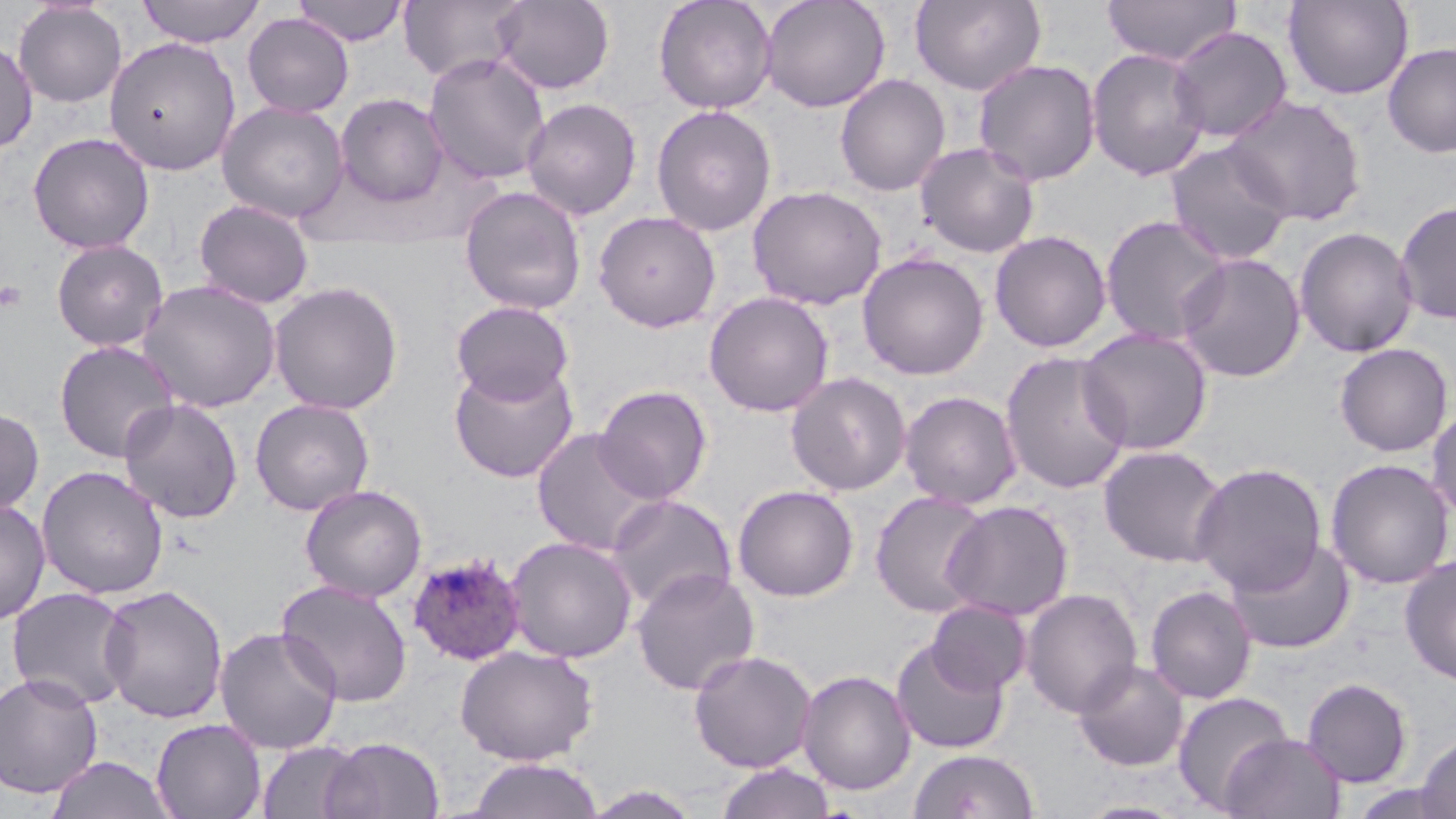 Approximate bounding boxes as (x1, y1, x2, y2) in pixels. Plasmodium ovale-infected red blood cell locations: (406, 552, 528, 667). Platelet locations: (0, 279, 27, 313). Uninfected red blood cell locations: (137, 0, 265, 47), (293, 0, 409, 46), (399, 0, 528, 84), (492, 0, 615, 95), (654, 0, 777, 113), (760, 0, 890, 112), (910, 0, 1048, 95), (1102, 0, 1241, 66), (1282, 0, 1414, 100), (13, 1, 127, 108), (242, 13, 355, 117), (1167, 26, 1292, 143), (103, 37, 240, 175), (0, 38, 38, 153), (1382, 42, 1456, 157), (1086, 48, 1210, 181), (423, 52, 551, 186), (973, 58, 1101, 186), (834, 74, 950, 195), (335, 93, 448, 207), (1225, 94, 1365, 227), (521, 97, 642, 220), (217, 101, 349, 224), (651, 104, 776, 237), (28, 132, 155, 254), (1165, 140, 1295, 266), (915, 141, 1041, 258), (747, 184, 886, 309), (459, 185, 587, 315), (194, 199, 315, 309), (1394, 199, 1456, 324), (593, 210, 722, 332), (1099, 214, 1231, 347), (1294, 226, 1419, 358), (989, 230, 1112, 352), (51, 238, 168, 351), (857, 251, 989, 380), (1175, 252, 1306, 382), (139, 280, 281, 412), (268, 281, 404, 415), (703, 291, 834, 417), (450, 300, 574, 405), (1077, 327, 1213, 455), (53, 340, 181, 463), (1334, 343, 1453, 457), (999, 351, 1133, 495), (448, 362, 579, 483), (786, 372, 912, 496), (594, 384, 712, 504), (899, 390, 1022, 510), (118, 398, 243, 523), (249, 398, 375, 516), (1426, 400, 1456, 524), (0, 407, 45, 518), (530, 427, 666, 557), (1098, 444, 1230, 568), (1325, 458, 1454, 589), (1190, 462, 1327, 596), (36, 466, 169, 600), (299, 484, 427, 602), (733, 484, 859, 601), (870, 490, 993, 617), (605, 494, 736, 613), (0, 498, 50, 626), (941, 500, 1074, 621), (505, 535, 638, 664), (1225, 537, 1355, 654), (1399, 554, 1456, 687), (630, 568, 761, 696), (275, 579, 413, 707), (98, 584, 229, 724), (1145, 585, 1257, 704), (6, 587, 136, 711), (1020, 587, 1143, 719), (926, 600, 1031, 697), (214, 626, 343, 754), (890, 637, 1011, 755), (455, 644, 599, 766), (688, 649, 817, 772), (1073, 659, 1189, 772), (796, 669, 917, 796), (0, 672, 103, 798), (1301, 677, 1413, 787), (1173, 692, 1293, 812), (151, 718, 267, 819), (1220, 732, 1346, 819), (1417, 733, 1456, 819), (320, 736, 445, 819), (257, 740, 364, 819), (907, 748, 1042, 819), (44, 756, 178, 819), (464, 757, 606, 818), (714, 761, 838, 819), (582, 785, 705, 818). Slide-level diagnosis: Plasmodium ovale. Thin blood smear. May-Grünwald-Giemsa-stained preparation. Captured at 1000x magnification. One field of a larger specimen. Optical microscopy. Image is 1456×819 pixels.